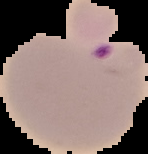
Summary:
  - Preparation: thin blood film
  - Image size: 148×154 pixels
  - Image type: segmented cell region with the area outside set to black
  - Malaria status: parasitized